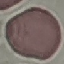

malaria status = uninfected
stain = Giemsa
image type = cell patch, automatically extracted from a larger field of view and resized to 64 × 64 pixels
capture = smartphone camera at the microscope eyepiece
preparation = thin blood smear